Give the preparation type.
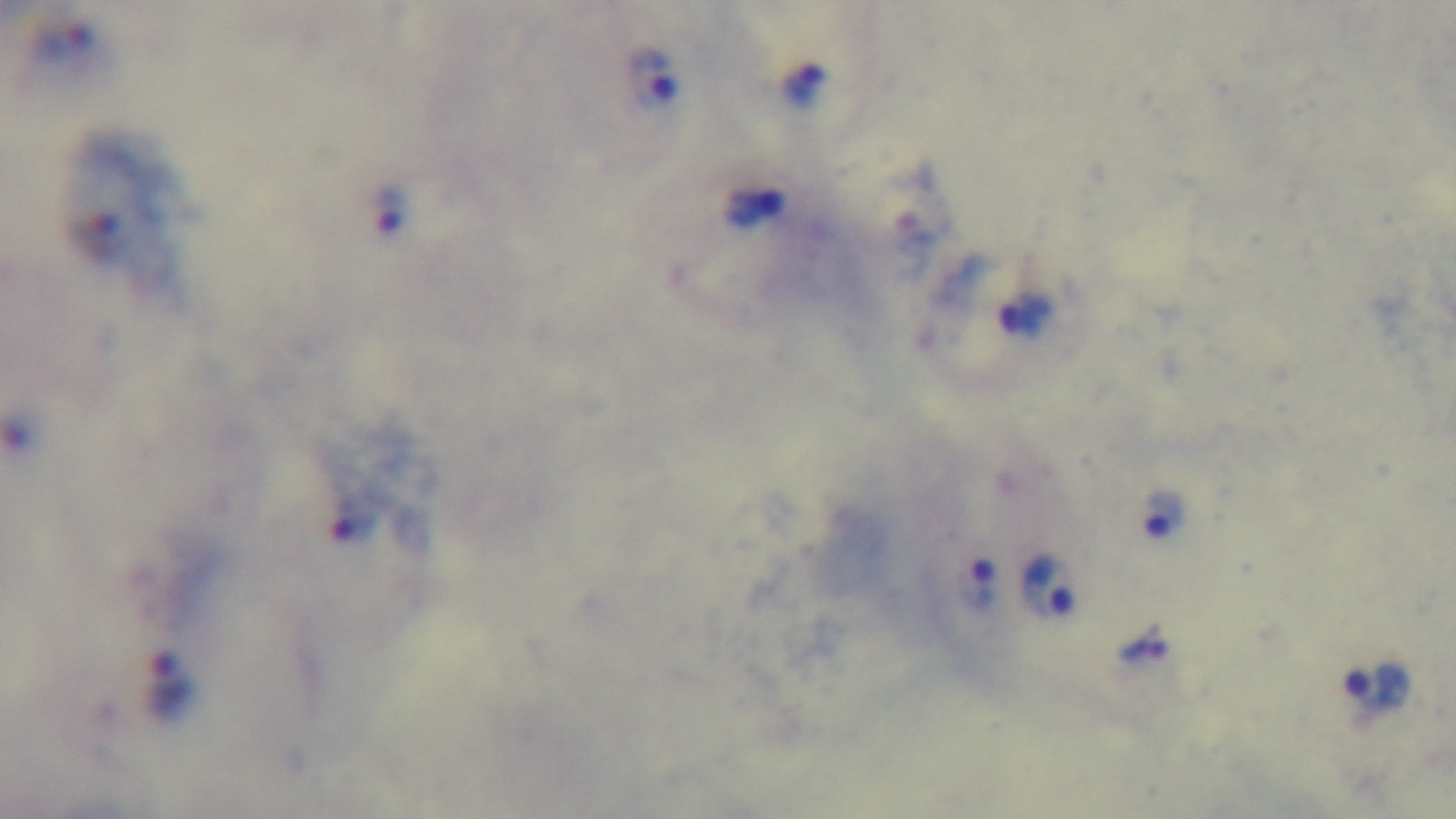
A thick smear.

Summary:
  - Field of view: single
  - Malaria status: infected
  - Modality: light microscopy
  - Capture: mounted 4K digital camera
  - Objective: 100x oil immersion
  - Stain: Giemsa